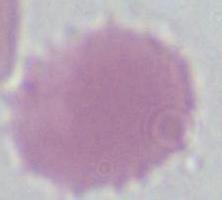
identification: red blood cell
magnification: 1000x
modality: photomicrograph